Assess the morphology of the red blood cells.
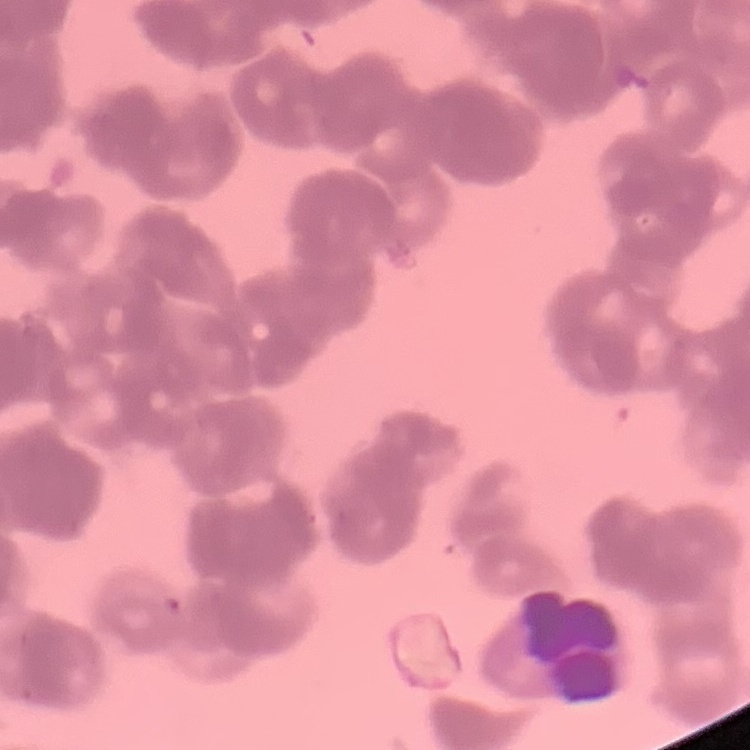
Rouleaux formation.

Thin blood film. Stained with either Field's or Giemsa. One tile cut from a larger photomicrograph.